Assess this cell for malaria.
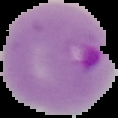
Parasitized.

Image is 118×118 pixels. From a thin blood smear. Cell region segmented out of the field of view; the surrounding area is masked to black.